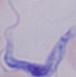
Summary:
  - Identification: trypanosome
  - Modality: photomicrograph
  - Magnification: 1000x